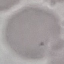

result = no malaria parasites seen
capture = smartphone through the microscope eyepiece
preparation = thin blood film
stain = Giemsa
image type = automatically extracted cell patch, resized to 64 × 64 pixels